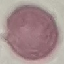
Malaria status: uninfected. Cell patch, automatically extracted from a larger field of view and resized to 64 × 64 pixels. Acquired by smartphone through the microscope eyepiece. Giemsa-stained preparation. Thin blood film.